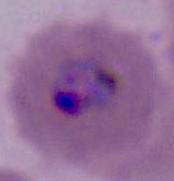

magnification: 400x or 1000x
modality: photomicrograph
identification: Plasmodium